Classify this cell by malaria status.
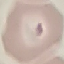

Parasitized.

Cell patch, automatically extracted from a larger field of view and resized to 64 × 64 pixels. Photographed with a smartphone camera at the microscope eyepiece. Giemsa stain. Thin smear of blood.